Report the malaria status of this cell.
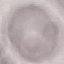

Uninfected.

capture = smartphone through the microscope eyepiece
stain = Giemsa
preparation = thin smear
image type = cell patch, automatically extracted from a larger field of view and resized to 64 × 64 pixels